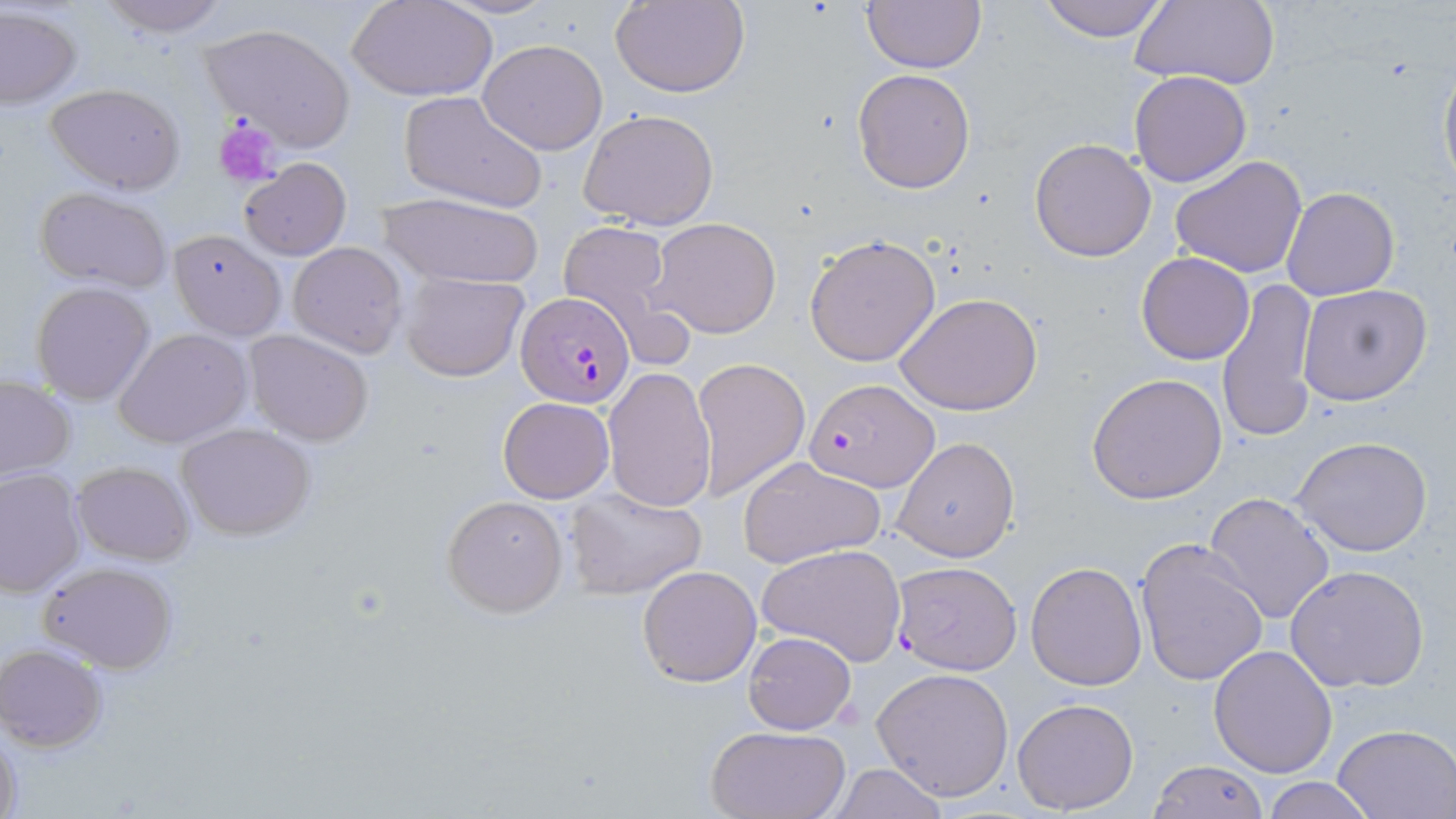 Approximate bounding boxes as (x1, y1, x2, y2) in pixels. Uninfected red blood cell locations: (95, 0, 234, 37), (432, 0, 561, 20), (611, 0, 750, 98), (1038, 0, 1170, 43), (1130, 0, 1282, 91), (349, 1, 496, 101), (862, 1, 985, 73), (1, 7, 81, 110), (198, 22, 357, 152), (477, 38, 608, 155), (1438, 54, 1456, 198), (436, 68, 613, 190), (852, 68, 976, 193), (1130, 71, 1252, 187), (42, 81, 188, 195), (398, 90, 547, 213), (578, 107, 719, 231), (1029, 137, 1157, 261), (1170, 155, 1308, 279), (239, 158, 351, 261), (1282, 186, 1400, 300), (33, 187, 174, 295), (375, 192, 546, 291), (649, 217, 781, 339), (558, 220, 676, 334), (167, 228, 287, 342), (805, 235, 940, 365), (287, 241, 409, 358), (1136, 251, 1256, 365), (400, 272, 529, 381), (1215, 277, 1322, 442), (31, 281, 157, 403), (1298, 282, 1433, 406), (895, 291, 1044, 416), (113, 328, 252, 448), (244, 328, 374, 447), (693, 359, 811, 502), (603, 365, 716, 513), (1086, 372, 1228, 504), (0, 375, 76, 483), (497, 396, 615, 503), (177, 421, 316, 540), (1291, 434, 1434, 557), (891, 436, 1020, 562), (738, 455, 886, 571), (71, 461, 194, 565), (0, 469, 86, 596), (565, 487, 708, 601), (1202, 492, 1335, 626), (442, 494, 569, 618), (1135, 538, 1270, 688), (757, 542, 907, 667), (38, 561, 179, 673), (1026, 561, 1148, 690), (636, 564, 763, 686), (1283, 564, 1432, 695), (744, 631, 856, 734), (1207, 643, 1338, 777), (0, 645, 107, 752), (872, 668, 1014, 801), (1012, 697, 1139, 815), (1333, 723, 1456, 817), (0, 725, 21, 819), (705, 725, 850, 818), (1147, 757, 1267, 818), (824, 763, 951, 819), (1262, 777, 1379, 818). Plasmodium falciparum-infected red blood cell locations: (516, 291, 637, 410), (804, 378, 938, 493), (891, 563, 1021, 676). Platelet locations: (215, 119, 282, 187). Slide-level diagnosis: Plasmodium falciparum. May-Grünwald-Giemsa-stained preparation. One field of a larger specimen. Image is 1456×819 pixels. 1000x magnification. Thin blood film. Light microscopy.